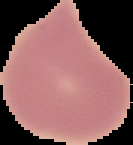

preparation: thin blood film
image_size: 133×145 pixels
image_type: segmented cell region with the area outside set to black
result: negative for Plasmodium parasites